Name the parasite shown.
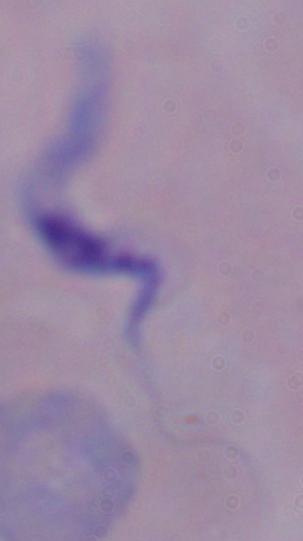
This is a trypanosome.

Summary:
  - Modality: photomicrograph
  - Magnification: 1000x